Assess this cell for malaria.
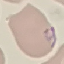
It is parasitized.

Giemsa stain. Cell patch, automatically extracted from a larger field of view and resized to 64 × 64 pixels. Acquired by smartphone through the microscope eyepiece. Thin blood film.